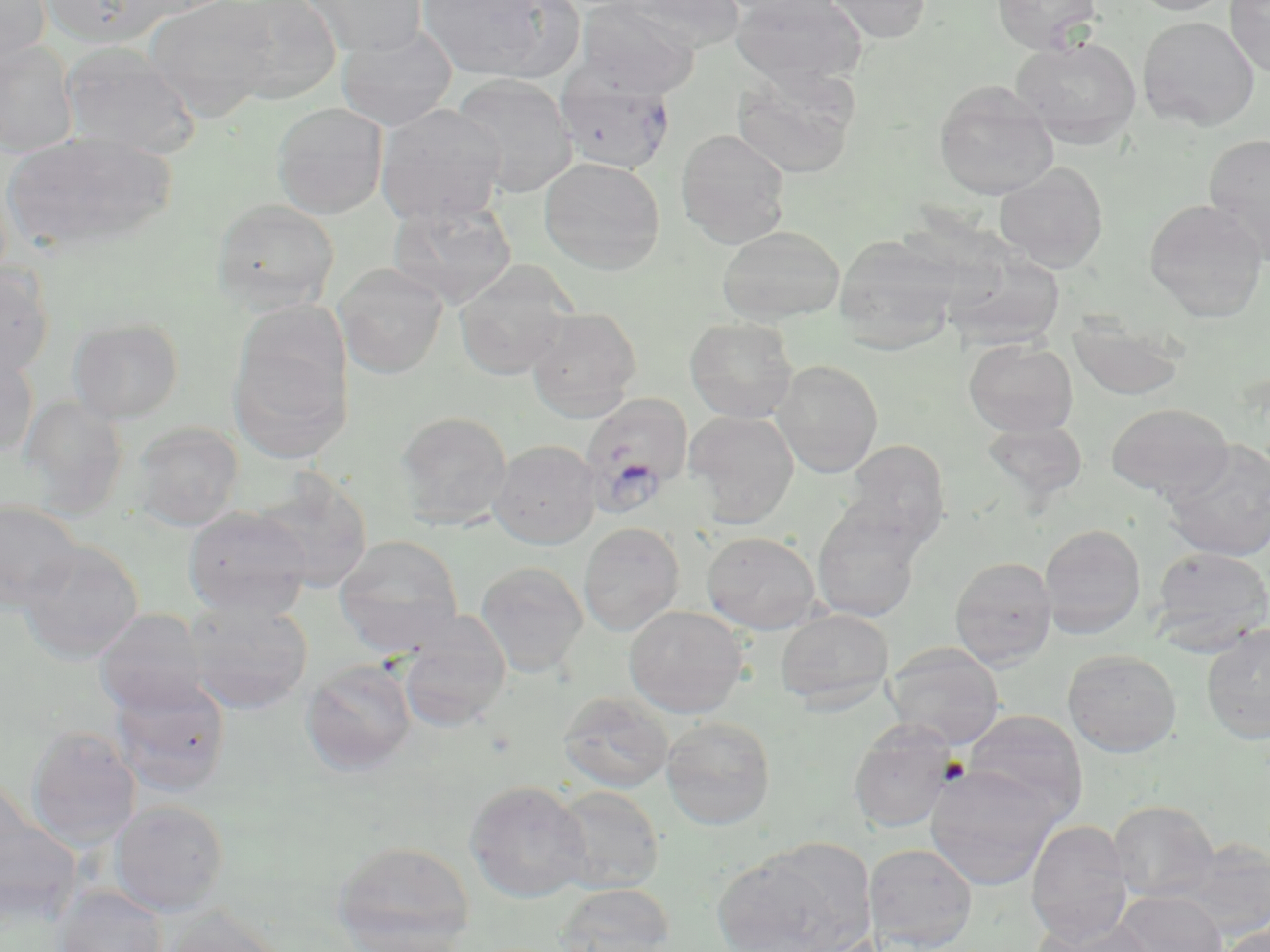

Approximate bounding boxes as named x1/y1/x2/y2 corners in pixels. Uninfected red blood cell locations: (x1=0, y1=0, x2=51, y2=66), (x1=38, y1=0, x2=177, y2=48), (x1=145, y1=0, x2=279, y2=121), (x1=217, y1=0, x2=342, y2=104), (x1=300, y1=0, x2=428, y2=58), (x1=418, y1=0, x2=550, y2=80), (x1=482, y1=0, x2=588, y2=84), (x1=614, y1=0, x2=745, y2=50), (x1=712, y1=0, x2=835, y2=18), (x1=730, y1=0, x2=867, y2=88), (x1=822, y1=0, x2=932, y2=44), (x1=991, y1=0, x2=1101, y2=55), (x1=1129, y1=0, x2=1234, y2=15), (x1=1225, y1=0, x2=1270, y2=77), (x1=575, y1=1, x2=700, y2=97), (x1=1137, y1=16, x2=1260, y2=131), (x1=336, y1=23, x2=458, y2=131), (x1=1011, y1=37, x2=1142, y2=148), (x1=0, y1=39, x2=79, y2=157), (x1=59, y1=41, x2=201, y2=158), (x1=730, y1=67, x2=860, y2=180), (x1=554, y1=72, x2=676, y2=174), (x1=451, y1=73, x2=578, y2=197), (x1=933, y1=80, x2=1059, y2=200), (x1=272, y1=102, x2=389, y2=219), (x1=375, y1=103, x2=506, y2=225), (x1=674, y1=129, x2=791, y2=247), (x1=3, y1=130, x2=175, y2=254), (x1=1203, y1=132, x2=1270, y2=262), (x1=539, y1=156, x2=666, y2=274), (x1=994, y1=162, x2=1108, y2=273), (x1=211, y1=198, x2=340, y2=312), (x1=388, y1=198, x2=518, y2=307), (x1=1144, y1=199, x2=1268, y2=322), (x1=716, y1=225, x2=846, y2=324), (x1=832, y1=234, x2=962, y2=352), (x1=940, y1=248, x2=1066, y2=349), (x1=453, y1=260, x2=577, y2=380), (x1=333, y1=263, x2=449, y2=378), (x1=0, y1=265, x2=54, y2=380), (x1=525, y1=307, x2=643, y2=421), (x1=1068, y1=316, x2=1188, y2=401), (x1=685, y1=317, x2=798, y2=423), (x1=68, y1=318, x2=184, y2=422), (x1=229, y1=332, x2=352, y2=463), (x1=963, y1=338, x2=1078, y2=437), (x1=0, y1=350, x2=39, y2=459), (x1=772, y1=359, x2=883, y2=477), (x1=18, y1=395, x2=129, y2=516), (x1=1106, y1=403, x2=1233, y2=499), (x1=395, y1=410, x2=513, y2=529), (x1=684, y1=410, x2=800, y2=527), (x1=981, y1=420, x2=1087, y2=507), (x1=131, y1=421, x2=244, y2=531), (x1=841, y1=439, x2=950, y2=550), (x1=1160, y1=439, x2=1270, y2=561), (x1=488, y1=440, x2=600, y2=549), (x1=251, y1=470, x2=374, y2=593), (x1=0, y1=500, x2=83, y2=611), (x1=812, y1=500, x2=929, y2=622), (x1=184, y1=506, x2=312, y2=619), (x1=578, y1=522, x2=684, y2=636), (x1=1039, y1=523, x2=1146, y2=638), (x1=701, y1=531, x2=822, y2=633), (x1=334, y1=534, x2=464, y2=655), (x1=18, y1=540, x2=144, y2=664), (x1=1150, y1=546, x2=1270, y2=653), (x1=950, y1=556, x2=1057, y2=668), (x1=475, y1=560, x2=588, y2=678), (x1=184, y1=597, x2=313, y2=714), (x1=624, y1=605, x2=748, y2=718), (x1=94, y1=608, x2=209, y2=715), (x1=775, y1=608, x2=894, y2=712), (x1=397, y1=617, x2=509, y2=732), (x1=1200, y1=623, x2=1270, y2=744), (x1=885, y1=642, x2=1006, y2=749), (x1=1063, y1=649, x2=1182, y2=756), (x1=301, y1=658, x2=417, y2=774), (x1=109, y1=676, x2=231, y2=798), (x1=557, y1=691, x2=674, y2=794), (x1=964, y1=710, x2=1087, y2=820), (x1=660, y1=716, x2=776, y2=830), (x1=848, y1=720, x2=957, y2=833), (x1=25, y1=725, x2=141, y2=849), (x1=926, y1=765, x2=1062, y2=890), (x1=466, y1=780, x2=593, y2=903), (x1=549, y1=785, x2=665, y2=895), (x1=108, y1=799, x2=230, y2=916), (x1=1109, y1=800, x2=1219, y2=902), (x1=1026, y1=820, x2=1133, y2=944), (x1=1174, y1=839, x2=1270, y2=942), (x1=332, y1=841, x2=477, y2=950), (x1=863, y1=842, x2=978, y2=951), (x1=715, y1=843, x2=871, y2=952), (x1=554, y1=882, x2=675, y2=952), (x1=54, y1=884, x2=168, y2=952), (x1=1113, y1=890, x2=1228, y2=952), (x1=159, y1=905, x2=286, y2=952), (x1=1031, y1=918, x2=1154, y2=952), (x1=1215, y1=923, x2=1270, y2=952), (x1=341, y1=931, x2=474, y2=952). Platelet locations: (x1=938, y1=757, x2=971, y2=785). Plasmodium falciparum-infected red blood cell locations: (x1=581, y1=391, x2=694, y2=514). Slide-level diagnosis: Plasmodium falciparum. Optical microscopy. Captured at 1000x magnification. Image is 1270×952 pixels. May-Grünwald-Giemsa-stained preparation. One field of a larger specimen. Thin blood smear.